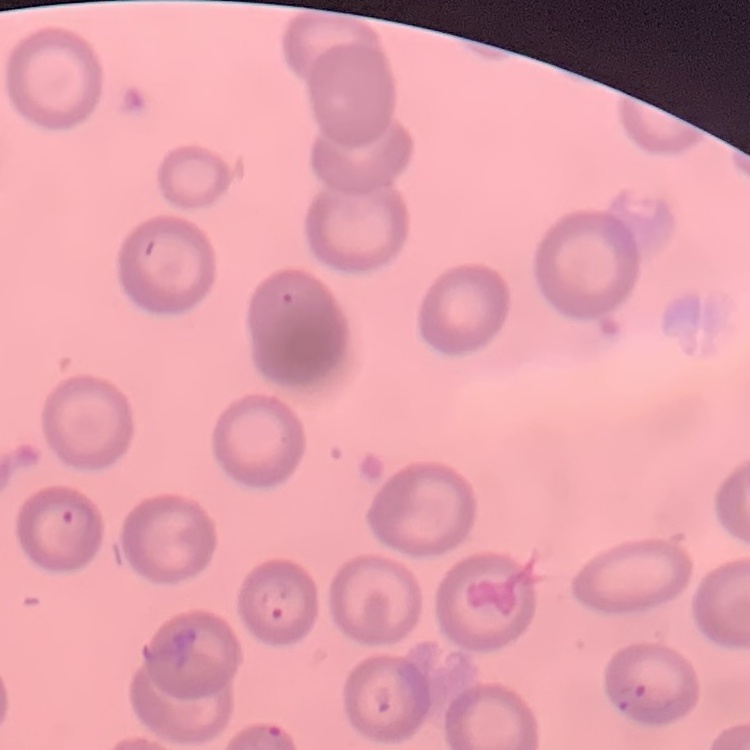
Summary:
  - Red blood cell morphology: no rouleaux formation
  - Preparation: thin blood film
  - Image type: one tile cut from a larger photomicrograph
  - Stain: Field's or Giemsa